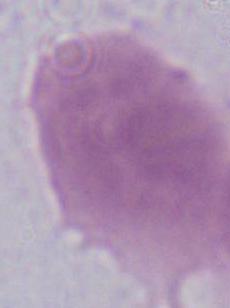

Summary:
  - Modality: micrograph
  - Identification: red blood cell
  - Magnification: 1000x